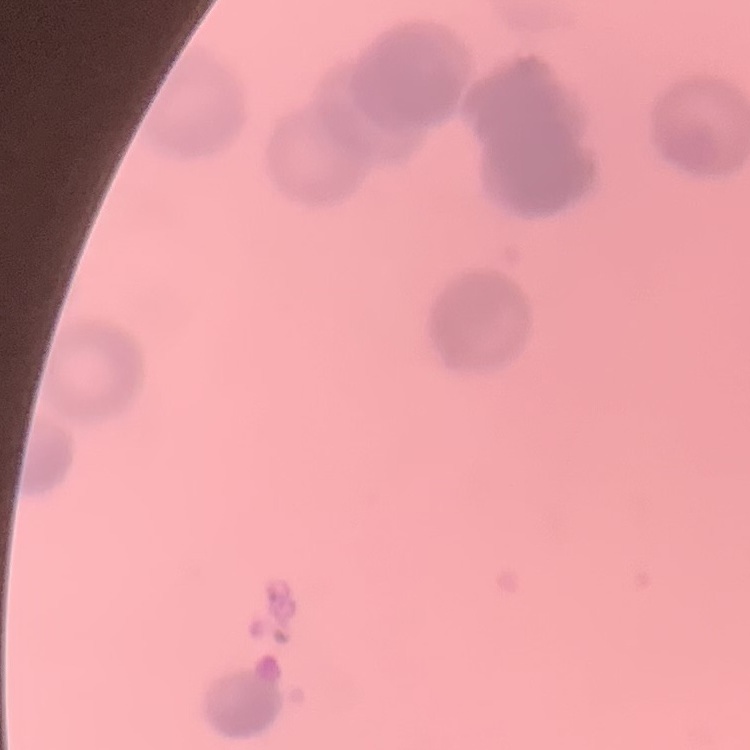
The erythrocytes show rouleaux formation. Square crop of a larger photomicrograph. Field's or Giemsa stain. Thin blood film.